Classify this cell by malaria status.
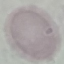

It is uninfected.

Summary:
  - Capture: smartphone camera at the microscope eyepiece
  - Image type: automatically extracted cell patch, resized to 64 × 64 pixels
  - Preparation: thin blood smear
  - Stain: Giemsa